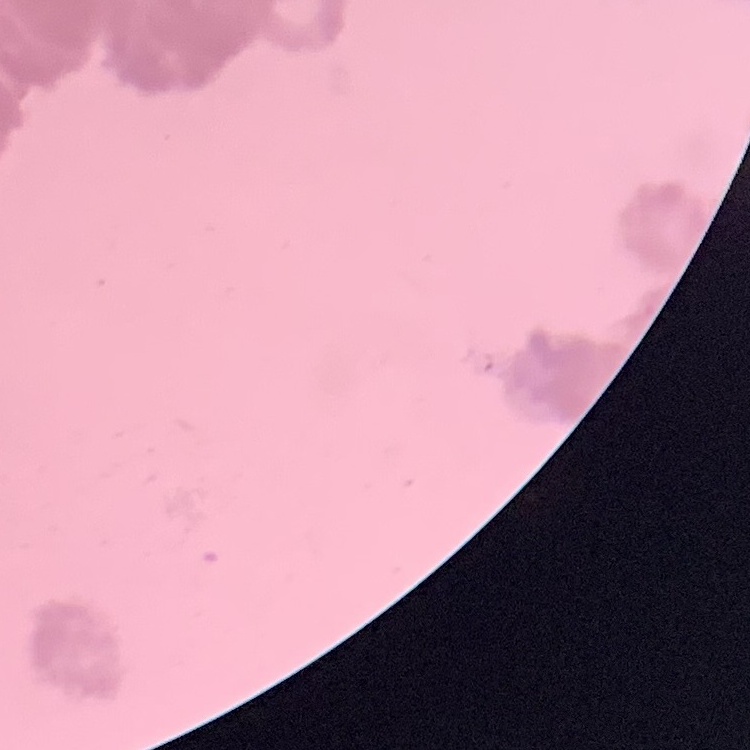
Summary:
  - Red blood cell morphology: rouleaux formation
  - Stain: Field's or Giemsa
  - Preparation: thin blood film
  - Image type: one tile cut from a larger photomicrograph